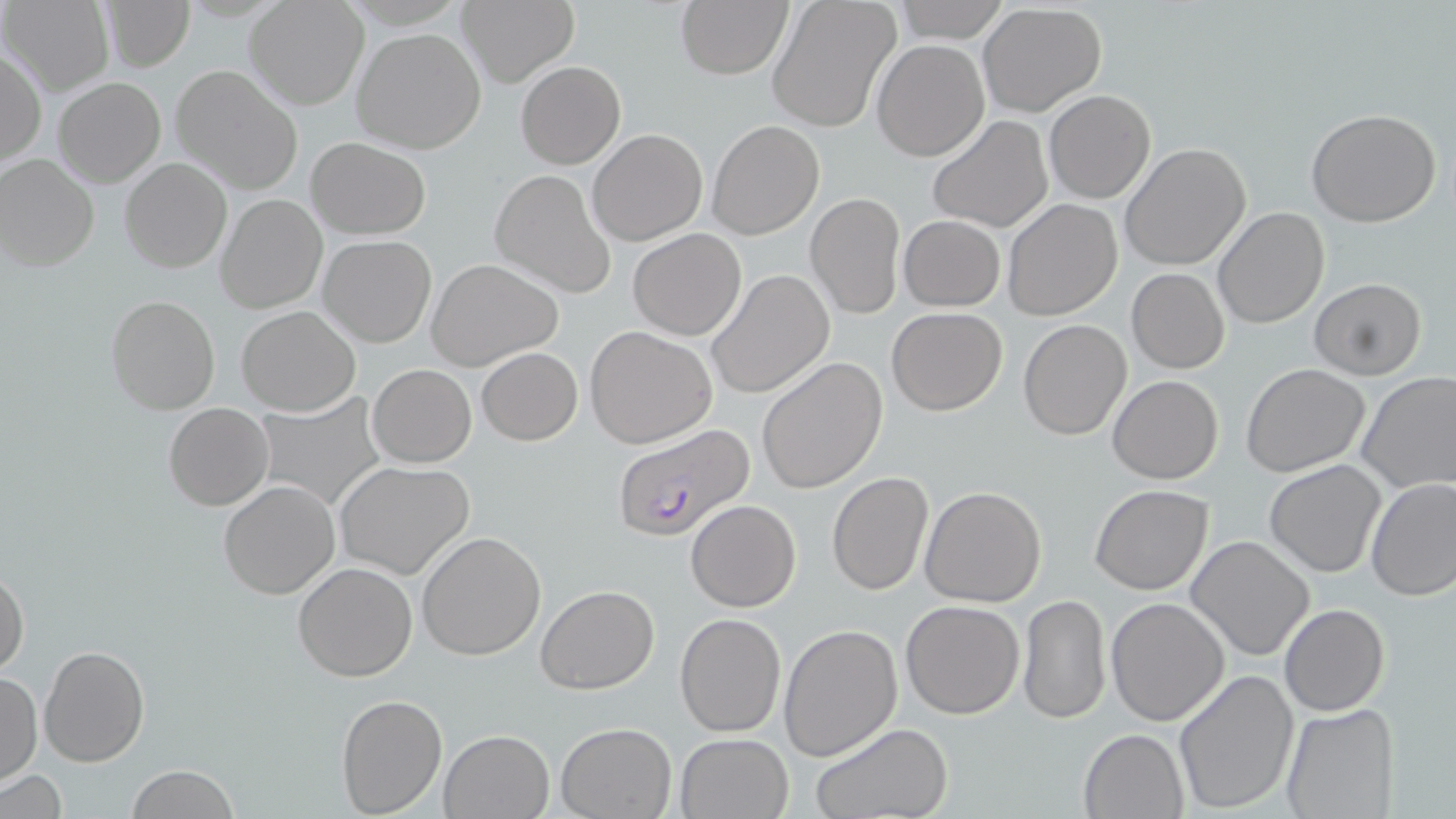
slide_level_diagnosis: Plasmodium falciparum
image_size: 1456×819 pixels
uninfected_red_blood_cell_locations: 'approximate bounding boxes as (x1,y1)-(x2,y2) corner pairs in pixels: (99,0)-(195,70), (457,0)-(579,88), (3,1)-(112,95), (676,1)-(793,79), (767,1)-(900,132), (892,1)-(1011,43), (244,3)-(367,111), (977,3)-(1108,117), (353,26)-(487,153), (872,39)-(989,161), (1,47)-(46,167), (516,62)-(625,168), (171,65)-(303,195), (54,76)-(165,187), (1044,90)-(1155,203), (1305,107)-(1443,227), (927,115)-(1054,234), (707,119)-(824,240), (588,128)-(708,246), (307,138)-(431,238), (1120,142)-(1251,271), (1,154)-(100,271), (120,157)-(231,273), (489,169)-(617,298), (807,192)-(905,320), (215,194)-(326,314), (1002,198)-(1124,321), (1212,206)-(1329,329), (899,215)-(1005,311), (628,229)-(747,340), (318,235)-(436,347), (426,258)-(563,371), (1127,268)-(1230,374), (706,269)-(835,398), (1308,278)-(1428,380), (106,295)-(220,416), (236,305)-(360,417), (887,307)-(1008,415), (1018,319)-(1133,440), (585,325)-(717,448), (476,347)-(582,445), (757,357)-(888,494), (368,364)-(476,467), (1241,364)-(1370,478), (1356,370)-(1456,494), (1107,375)-(1223,485), (253,395)-(384,510), (163,402)-(273,511), (1264,459)-(1387,578), (335,460)-(476,580), (826,472)-(933,594), (1366,478)-(1456,603), (218,481)-(340,600), (1090,484)-(1213,595), (919,486)-(1046,607), (685,499)-(801,611), (416,532)-(547,661), (1186,535)-(1315,661), (293,562)-(418,683), (0,566)-(30,680), (535,585)-(658,695), (1018,594)-(1110,724), (1106,596)-(1230,726), (899,600)-(1025,719), (1279,603)-(1390,716), (675,611)-(787,738), (778,623)-(903,762), (40,646)-(148,766), (1171,669)-(1298,815), (1,670)-(42,786), (336,692)-(448,817), (1280,703)-(1400,818), (810,721)-(957,819), (554,722)-(676,818), (1078,728)-(1189,819), (440,729)-(553,817), (674,731)-(794,819), (125,766)-(240,819), (2,772)-(69,818)'
preparation: thin blood film
modality: light microscopy
stain: May-Grünwald-Giemsa
plasmodium_falciparum_infected_red_blood_cell_locations: 'approximate bounding boxes as (x1,y1)-(x2,y2) corner pairs in pixels: (611,423)-(756,544)'
field_of_view: single
magnification: 1000x